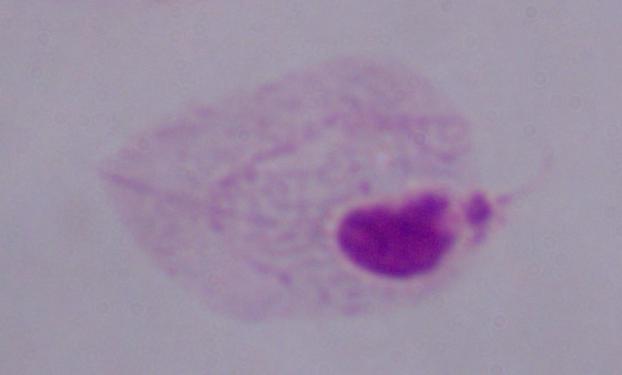
Summary:
  - Identification: trichomonad
  - Modality: micrograph
  - Magnification: 1000x